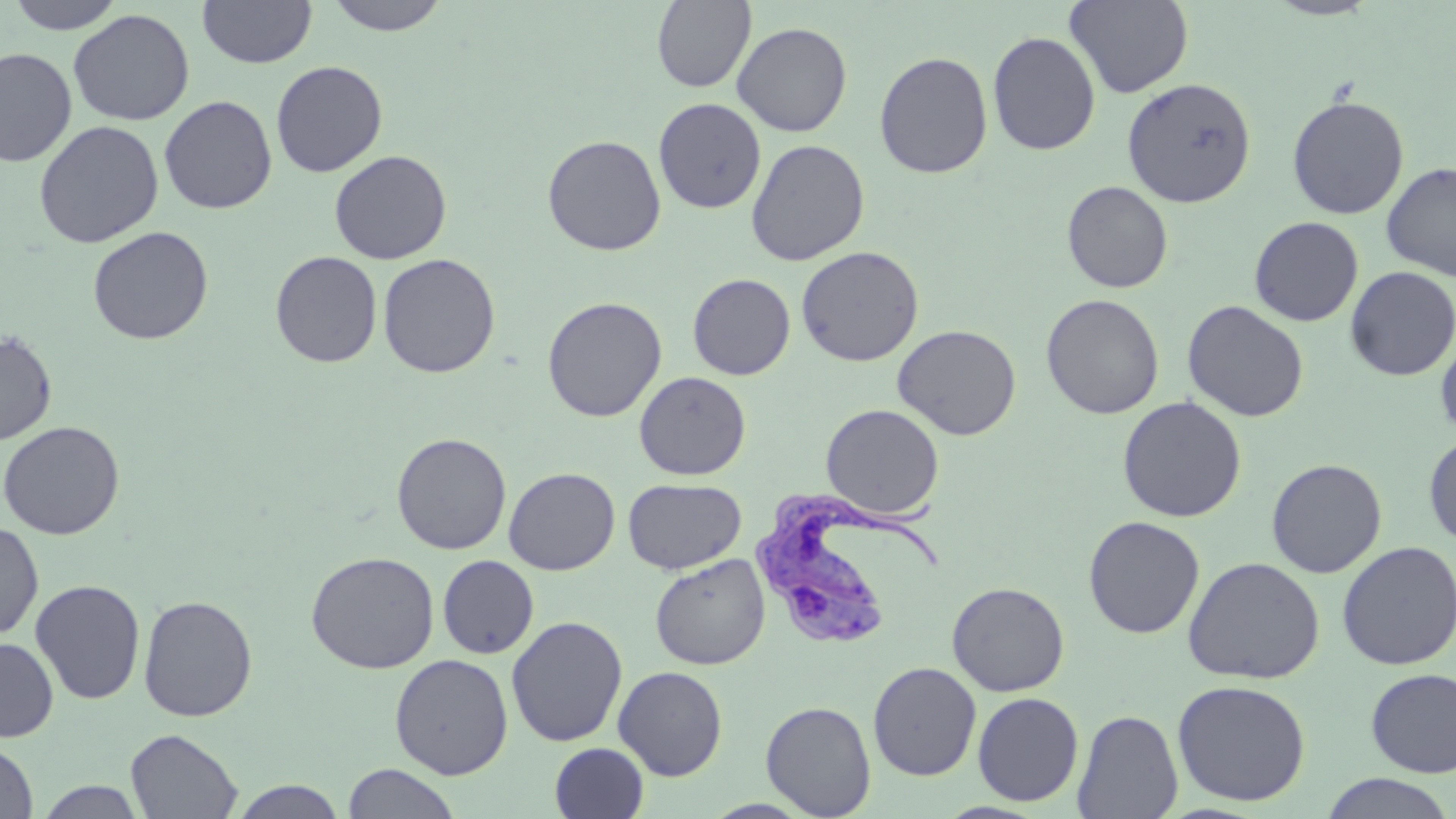
Approximate bounding boxes as [x1, y1, x2, y2] in pixels. Trypanosoma brucei locations: [751, 481, 943, 649]. Uninfected red blood cell locations: [6, 0, 129, 33], [197, 0, 317, 68], [324, 0, 451, 35], [1065, 0, 1193, 98], [1263, 0, 1383, 20], [652, 1, 756, 92], [68, 9, 194, 126], [732, 21, 852, 137], [987, 31, 1101, 156], [0, 47, 76, 167], [874, 51, 993, 179], [271, 60, 388, 178], [1122, 78, 1256, 208], [1286, 95, 1409, 219], [159, 96, 277, 215], [653, 98, 767, 213], [33, 120, 164, 248], [542, 134, 666, 255], [745, 139, 870, 266], [329, 149, 452, 265], [1381, 162, 1456, 280], [1061, 181, 1173, 293], [1248, 216, 1364, 327], [87, 226, 213, 344], [796, 246, 924, 366], [270, 251, 382, 368], [377, 253, 501, 378], [1345, 266, 1456, 380], [687, 273, 796, 380], [1041, 294, 1164, 419], [542, 296, 667, 421], [1182, 300, 1309, 422], [892, 323, 1022, 441], [0, 331, 58, 445], [1435, 331, 1456, 440], [634, 371, 751, 480], [1117, 396, 1247, 523], [821, 404, 944, 519], [0, 420, 124, 540], [392, 433, 512, 555], [1423, 433, 1456, 548], [1266, 458, 1387, 578], [504, 467, 620, 575], [623, 478, 746, 575], [1082, 515, 1205, 639], [0, 521, 43, 640], [1336, 540, 1456, 670], [305, 551, 440, 673], [650, 553, 770, 670], [437, 555, 539, 658], [1182, 556, 1325, 684], [29, 579, 145, 705], [946, 581, 1070, 696], [138, 594, 258, 722], [506, 615, 627, 747], [0, 636, 59, 742], [390, 653, 513, 779], [868, 661, 982, 781], [613, 665, 728, 780], [1365, 668, 1456, 778], [1171, 679, 1311, 806], [972, 692, 1083, 806], [761, 700, 877, 818], [1072, 709, 1184, 818], [126, 728, 242, 818], [0, 740, 38, 818], [549, 743, 649, 819], [342, 763, 461, 819], [1320, 773, 1453, 818], [229, 780, 348, 819], [35, 781, 147, 818]. Slide-level diagnosis: Trypanosoma brucei. Thin blood smear. Light microscopy. 1000x magnification. May-Grünwald-Giemsa-stained preparation. Image is 1456×819 pixels. One field of a larger specimen.